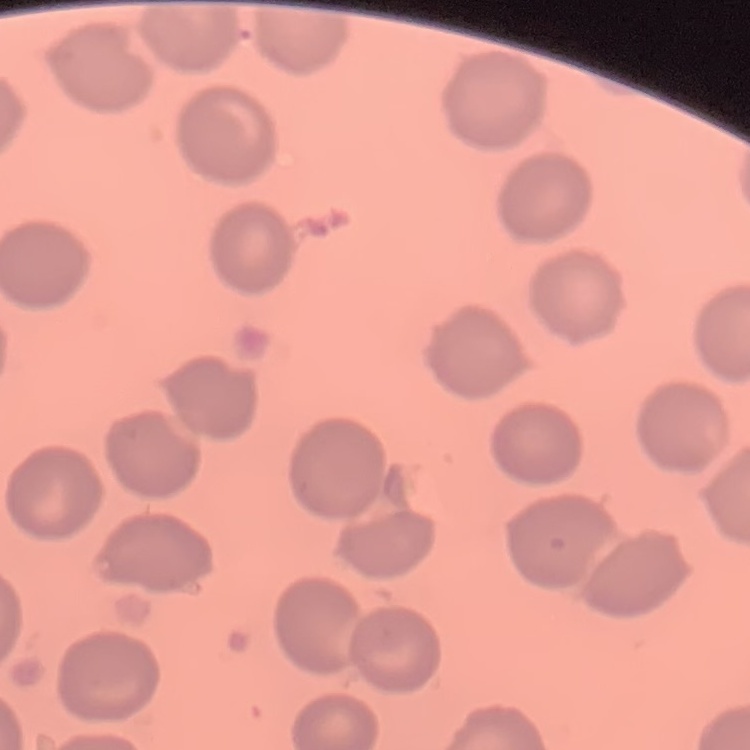
The erythrocytes show no rouleaux formation. Thin blood film. One tile cut from a larger photomicrograph. Stained with either Field's or Giemsa.